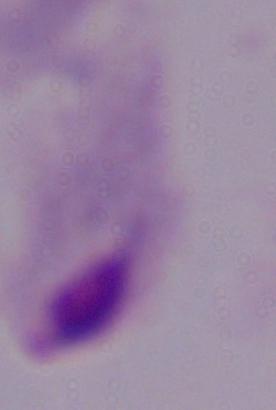

Micrograph. A trichomonad is shown. Captured at 1000x magnification.